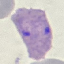
Malaria status: parasitized. Thin smear of blood. Cell patch, automatically extracted from a larger field of view and resized to 64 × 64 pixels. Acquired by smartphone through the microscope eyepiece. Giemsa stain.